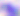

Toxoplasma gondii is shown. Photomicrograph. Captured at 400x magnification.